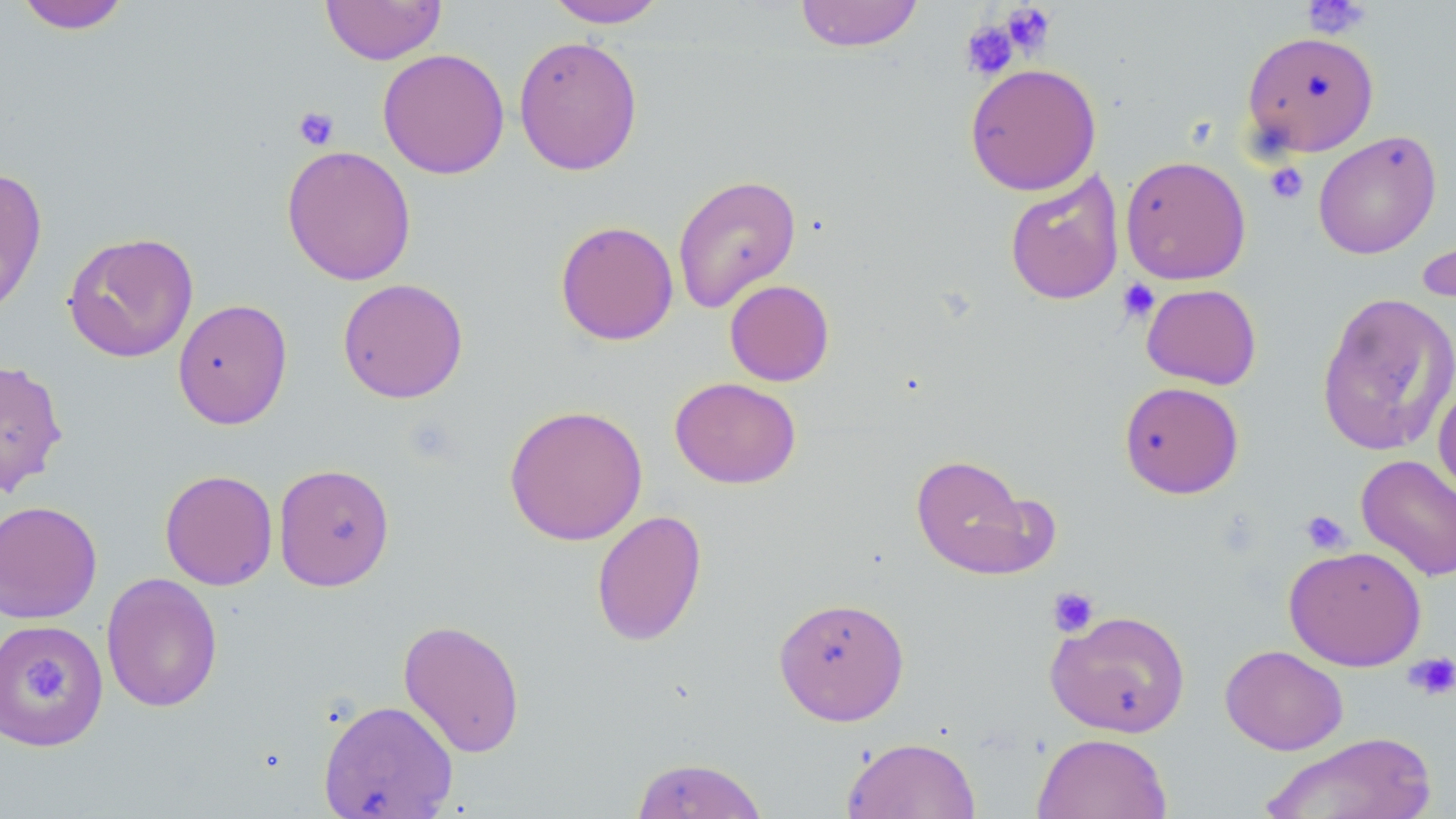 Approximate bounding boxes as named x1/y1/x2/y2 corners in pixels. Uninfected red blood cell locations: (x1=321, y1=0, x2=446, y2=65), (x1=544, y1=0, x2=669, y2=28), (x1=794, y1=0, x2=923, y2=52), (x1=15, y1=1, x2=131, y2=34), (x1=1241, y1=30, x2=1379, y2=157), (x1=513, y1=35, x2=643, y2=175), (x1=377, y1=48, x2=510, y2=179), (x1=964, y1=62, x2=1102, y2=196), (x1=1313, y1=130, x2=1442, y2=259), (x1=281, y1=145, x2=417, y2=285), (x1=1120, y1=155, x2=1252, y2=285), (x1=0, y1=167, x2=48, y2=317), (x1=1004, y1=170, x2=1125, y2=306), (x1=672, y1=173, x2=802, y2=313), (x1=555, y1=220, x2=678, y2=345), (x1=1417, y1=229, x2=1455, y2=315), (x1=62, y1=231, x2=199, y2=363), (x1=337, y1=278, x2=468, y2=403), (x1=724, y1=279, x2=835, y2=386), (x1=1141, y1=283, x2=1262, y2=389), (x1=1316, y1=291, x2=1456, y2=457), (x1=172, y1=298, x2=293, y2=430), (x1=0, y1=358, x2=68, y2=497), (x1=670, y1=376, x2=801, y2=489), (x1=1433, y1=379, x2=1456, y2=501), (x1=1119, y1=381, x2=1244, y2=499), (x1=503, y1=404, x2=649, y2=546), (x1=910, y1=454, x2=1046, y2=579), (x1=1355, y1=454, x2=1456, y2=581), (x1=273, y1=463, x2=395, y2=591), (x1=159, y1=469, x2=278, y2=590), (x1=0, y1=500, x2=102, y2=625), (x1=591, y1=510, x2=707, y2=646), (x1=1283, y1=545, x2=1427, y2=671), (x1=100, y1=572, x2=223, y2=713), (x1=773, y1=595, x2=910, y2=726), (x1=1046, y1=609, x2=1191, y2=737), (x1=398, y1=618, x2=526, y2=758), (x1=0, y1=620, x2=109, y2=751), (x1=1220, y1=644, x2=1348, y2=755), (x1=318, y1=699, x2=458, y2=819), (x1=1032, y1=732, x2=1173, y2=819), (x1=1259, y1=732, x2=1438, y2=818), (x1=842, y1=736, x2=981, y2=819), (x1=630, y1=756, x2=770, y2=818). Platelet locations: (x1=1301, y1=0, x2=1372, y2=40), (x1=999, y1=2, x2=1057, y2=57), (x1=960, y1=19, x2=1020, y2=80), (x1=293, y1=105, x2=340, y2=151), (x1=1265, y1=162, x2=1309, y2=204), (x1=1117, y1=278, x2=1160, y2=324), (x1=1300, y1=509, x2=1351, y2=555), (x1=1047, y1=586, x2=1100, y2=637), (x1=1404, y1=651, x2=1456, y2=700), (x1=21, y1=659, x2=74, y2=704). Slide-level diagnosis: no evidence of blood parasites. 1000x magnification. One field of a larger specimen. Thin blood smear. May-Grünwald-Giemsa-stained preparation. Light microscopy. Image is 1456×819 pixels.